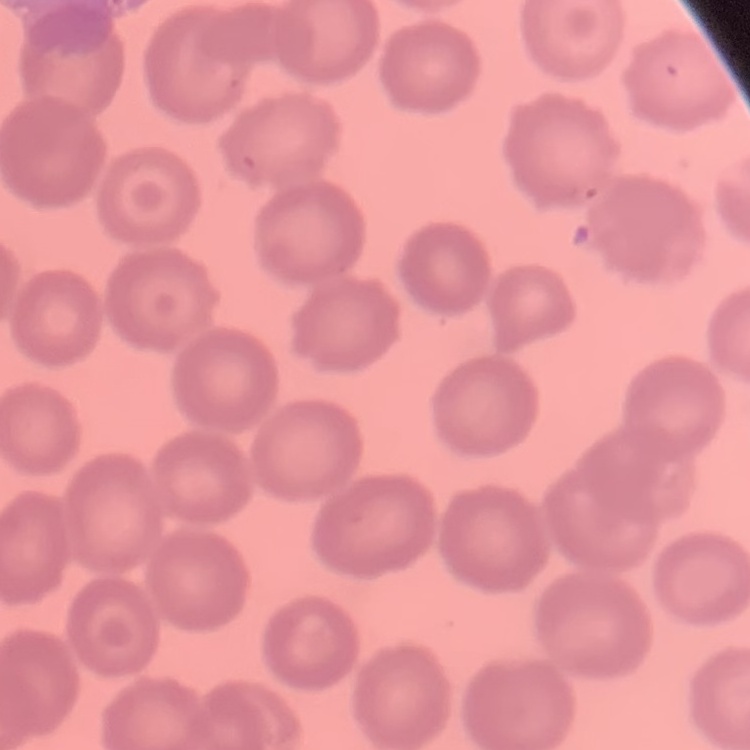 The red blood cells show no rouleaux formation. One tile cut from a larger photomicrograph. Thin blood film. Field's or Giemsa stain.